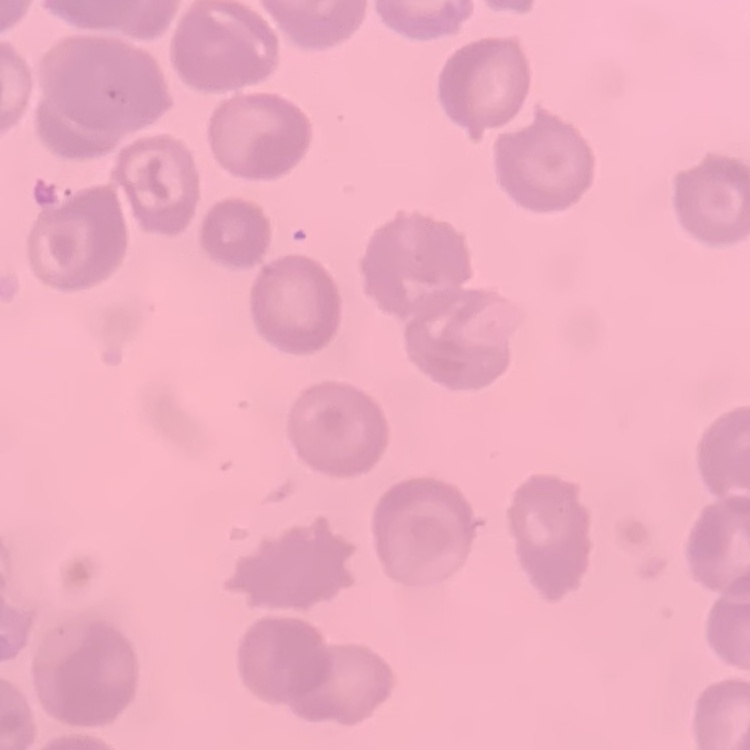 The erythrocytes exhibit no rouleaux formation. Field's or Giemsa stain. Square crop of a larger photomicrograph. Thin peripheral smear.